Locate and identify every blood parasite.
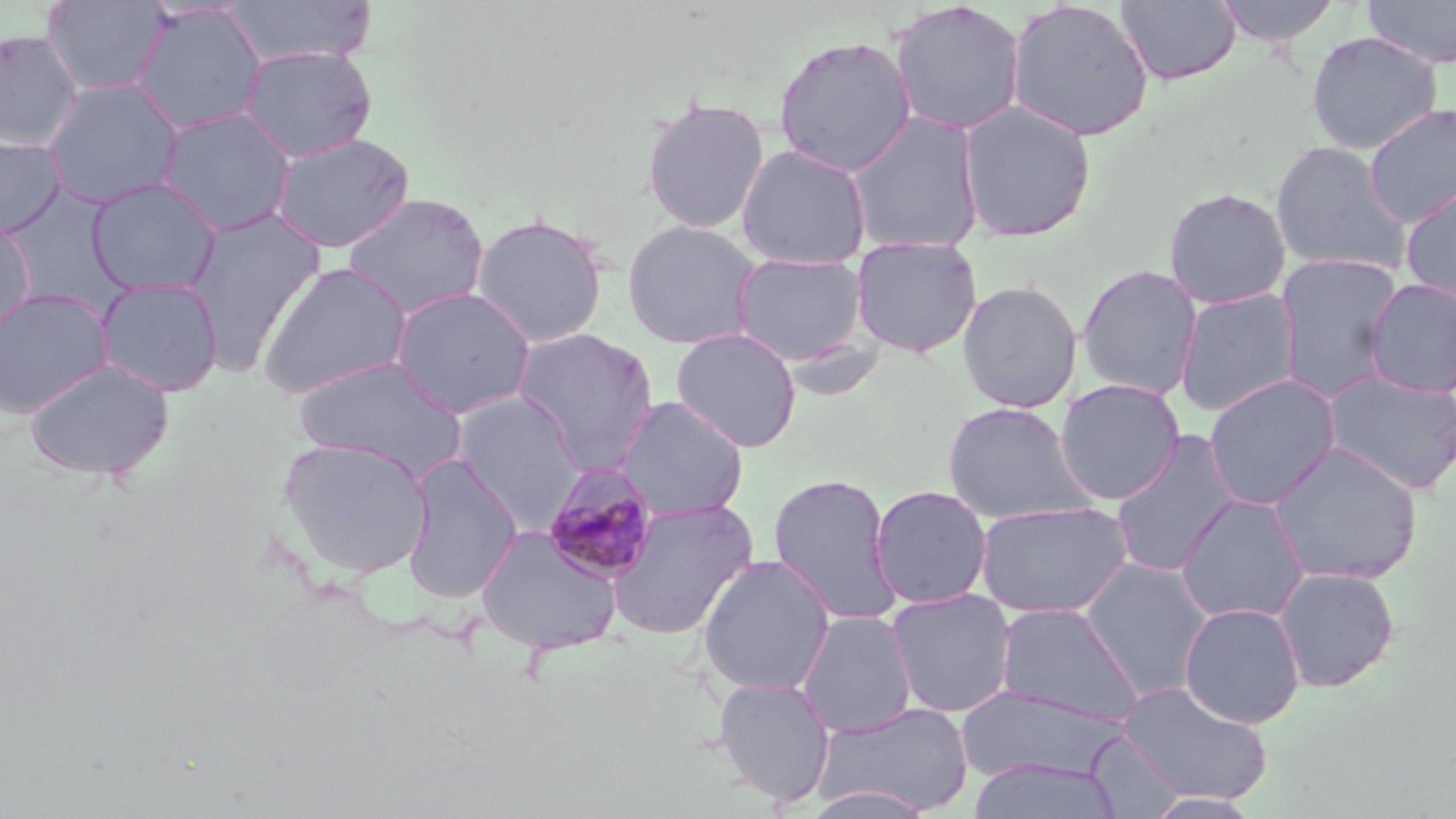

Approximate bounding boxes as (x1,y1)-(x2,y2) corner pairs in pixels.
Plasmodium malariae-infected red blood cells: (541,462)-(661,583).
No Plasmodium falciparum, Plasmodium ovale, Plasmodium vivax, Babesia divergens, or Trypanosoma brucei observed.

Summary:
  - Uninfected red blood cell locations: (40,0)-(173,97), (222,0)-(378,67), (1115,0)-(1242,86), (1213,0)-(1344,47), (1363,0)-(1456,68), (889,1)-(1026,137), (1005,1)-(1154,143), (130,4)-(267,135), (0,29)-(82,150), (1306,31)-(1442,155), (773,33)-(918,177), (239,45)-(378,162), (42,76)-(185,208), (640,96)-(770,234), (957,100)-(1097,242), (1363,103)-(1456,228), (158,107)-(297,236), (845,110)-(985,254), (269,133)-(415,253), (0,135)-(66,237), (1270,140)-(1411,276), (735,143)-(873,269), (86,177)-(222,298), (1399,182)-(1456,306), (2,187)-(131,311), (1163,187)-(1291,309), (341,192)-(490,320), (182,207)-(326,375), (471,213)-(609,347), (621,219)-(763,350), (0,221)-(35,337), (850,236)-(983,357), (731,251)-(869,365), (1274,252)-(1405,402), (257,261)-(413,398), (1076,264)-(1203,401), (95,277)-(224,396), (1363,278)-(1456,398), (957,281)-(1083,413), (389,286)-(538,419), (0,288)-(114,417), (1175,288)-(1301,417), (511,327)-(660,471), (671,327)-(802,453), (295,356)-(469,479), (24,358)-(175,481), (1322,369)-(1456,495), (1203,373)-(1340,510), (1054,378)-(1185,505), (452,392)-(585,526), (614,395)-(750,521), (942,401)-(1095,524), (1109,428)-(1243,578), (277,436)-(435,579), (1266,441)-(1423,587), (401,454)-(524,603), (767,473)-(903,626), (869,485)-(993,609), (1175,493)-(1311,625), (604,499)-(759,641), (975,499)-(1134,619), (474,524)-(625,655), (697,553)-(836,695), (1081,558)-(1214,701), (1273,566)-(1400,693), (886,587)-(1018,718), (994,602)-(1143,727), (1178,602)-(1306,728), (796,609)-(917,738), (713,676)-(837,807), (1116,680)-(1273,805), (957,685)-(1124,784), (813,701)-(975,817), (1086,731)-(1185,817), (967,757)-(1122,819), (803,784)-(938,819), (1142,792)-(1262,818)
  - Slide-level diagnosis: Plasmodium malariae
  - Field of view: one of a larger specimen
  - Image size: 1456×819 pixels
  - Magnification: 1000x
  - Preparation: thin blood smear
  - Modality: light microscopy
  - Stain: May-Grünwald-Giemsa